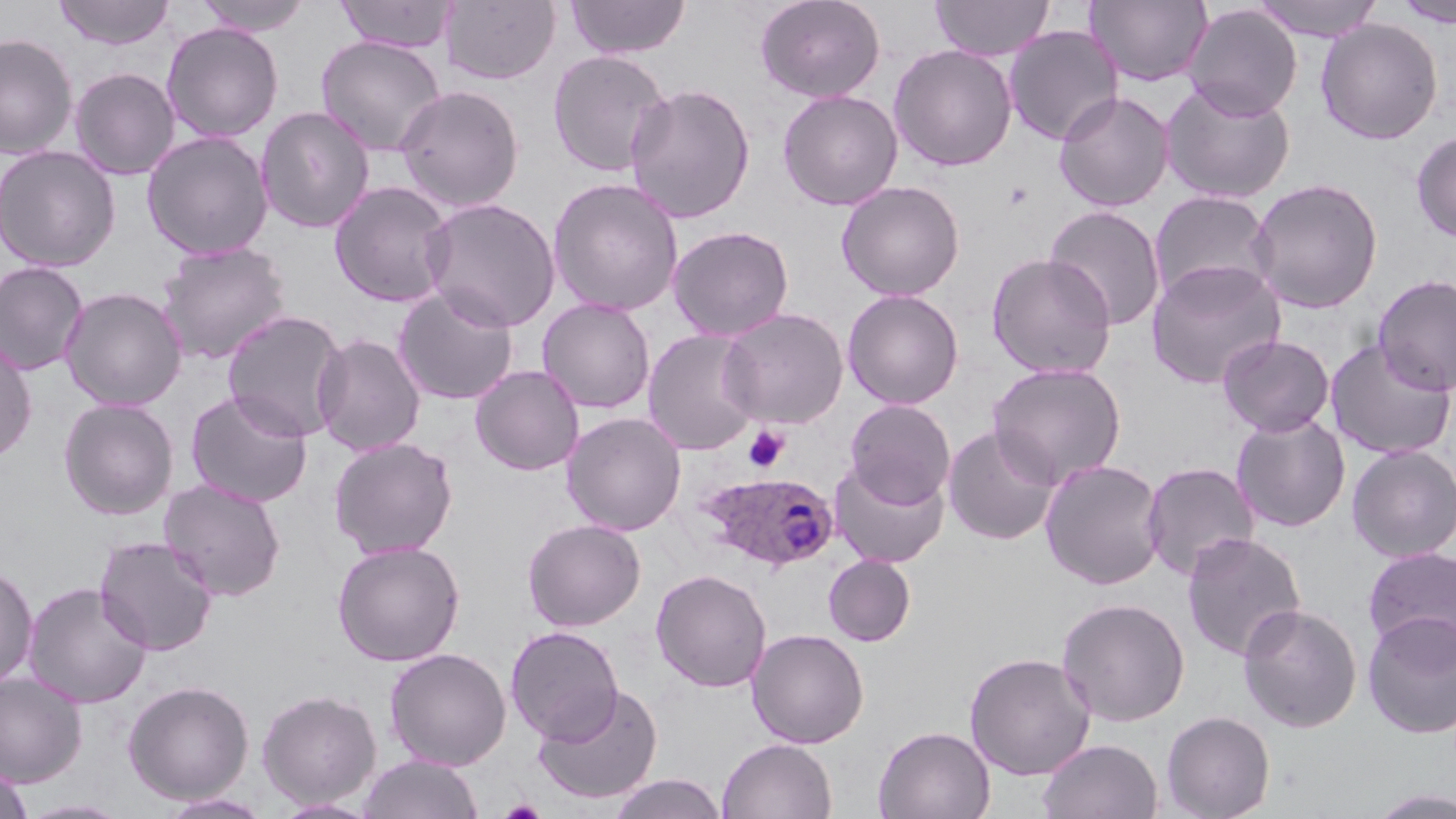
Summary:
  - Coordinate format: approximate bounding boxes as named x1/y1/x2/y2 corners in pixels
  - Platelet locations: (x1=744, y1=426, x2=789, y2=472)
  - Plasmodium ovale-infected red blood cell locations: (x1=696, y1=472, x2=839, y2=571)
  - Uninfected red blood cell locations: (x1=53, y1=0, x2=175, y2=50), (x1=193, y1=0, x2=313, y2=36), (x1=334, y1=0, x2=458, y2=53), (x1=566, y1=0, x2=691, y2=59), (x1=755, y1=0, x2=886, y2=102), (x1=931, y1=0, x2=1054, y2=61), (x1=1085, y1=0, x2=1213, y2=87), (x1=1251, y1=0, x2=1384, y2=41), (x1=440, y1=1, x2=561, y2=86), (x1=1394, y1=1, x2=1456, y2=28), (x1=1183, y1=4, x2=1302, y2=120), (x1=1316, y1=18, x2=1443, y2=145), (x1=161, y1=22, x2=283, y2=143), (x1=1003, y1=26, x2=1123, y2=146), (x1=0, y1=33, x2=78, y2=159), (x1=316, y1=36, x2=446, y2=157), (x1=888, y1=44, x2=1018, y2=172), (x1=547, y1=50, x2=671, y2=177), (x1=69, y1=67, x2=180, y2=180), (x1=1159, y1=80, x2=1296, y2=204), (x1=624, y1=83, x2=756, y2=224), (x1=394, y1=84, x2=524, y2=212), (x1=777, y1=89, x2=903, y2=210), (x1=1053, y1=90, x2=1175, y2=212), (x1=255, y1=105, x2=375, y2=234), (x1=1411, y1=130, x2=1456, y2=243), (x1=141, y1=131, x2=274, y2=259), (x1=0, y1=144, x2=121, y2=273), (x1=548, y1=177, x2=685, y2=316), (x1=1248, y1=177, x2=1384, y2=314), (x1=836, y1=180, x2=965, y2=301), (x1=330, y1=181, x2=455, y2=307), (x1=1149, y1=190, x2=1276, y2=306), (x1=421, y1=197, x2=561, y2=332), (x1=1044, y1=205, x2=1167, y2=330), (x1=667, y1=225, x2=794, y2=341), (x1=157, y1=242, x2=292, y2=364), (x1=985, y1=253, x2=1117, y2=379), (x1=1145, y1=259, x2=1286, y2=389), (x1=0, y1=261, x2=90, y2=376), (x1=1373, y1=273, x2=1456, y2=397), (x1=392, y1=286, x2=520, y2=405), (x1=59, y1=287, x2=188, y2=411), (x1=842, y1=288, x2=964, y2=409), (x1=537, y1=297, x2=656, y2=414), (x1=717, y1=307, x2=849, y2=429), (x1=221, y1=310, x2=348, y2=442), (x1=643, y1=329, x2=763, y2=455), (x1=312, y1=333, x2=426, y2=456), (x1=1217, y1=334, x2=1335, y2=437), (x1=0, y1=338, x2=37, y2=463), (x1=1326, y1=338, x2=1455, y2=460), (x1=987, y1=362, x2=1127, y2=487), (x1=470, y1=364, x2=585, y2=475), (x1=184, y1=389, x2=314, y2=508), (x1=58, y1=398, x2=179, y2=520), (x1=845, y1=400, x2=956, y2=507), (x1=561, y1=412, x2=686, y2=536), (x1=1231, y1=412, x2=1351, y2=533), (x1=943, y1=424, x2=1060, y2=545), (x1=328, y1=437, x2=459, y2=559), (x1=1347, y1=443, x2=1456, y2=562), (x1=829, y1=459, x2=950, y2=569), (x1=1040, y1=459, x2=1167, y2=589), (x1=1141, y1=461, x2=1259, y2=581), (x1=158, y1=478, x2=287, y2=601), (x1=523, y1=519, x2=646, y2=631), (x1=1181, y1=532, x2=1307, y2=661), (x1=94, y1=536, x2=218, y2=656), (x1=331, y1=539, x2=466, y2=666), (x1=1362, y1=546, x2=1456, y2=660), (x1=823, y1=554, x2=916, y2=647), (x1=0, y1=564, x2=38, y2=688), (x1=650, y1=569, x2=772, y2=693), (x1=23, y1=582, x2=152, y2=709), (x1=1056, y1=597, x2=1190, y2=727), (x1=1237, y1=604, x2=1362, y2=733), (x1=1362, y1=611, x2=1456, y2=739), (x1=506, y1=625, x2=624, y2=743), (x1=747, y1=627, x2=869, y2=748), (x1=384, y1=647, x2=512, y2=770), (x1=965, y1=652, x2=1096, y2=780), (x1=0, y1=672, x2=86, y2=787), (x1=122, y1=680, x2=255, y2=804), (x1=363, y1=681, x2=501, y2=817), (x1=532, y1=683, x2=664, y2=805), (x1=256, y1=689, x2=381, y2=808), (x1=1161, y1=711, x2=1276, y2=819), (x1=874, y1=725, x2=995, y2=819), (x1=717, y1=738, x2=837, y2=819), (x1=1037, y1=738, x2=1163, y2=819), (x1=357, y1=754, x2=483, y2=819), (x1=0, y1=767, x2=34, y2=819), (x1=606, y1=773, x2=728, y2=819), (x1=1366, y1=789, x2=1456, y2=818), (x1=158, y1=792, x2=272, y2=818), (x1=19, y1=798, x2=133, y2=818), (x1=270, y1=798, x2=381, y2=818)
  - Slide-level diagnosis: Plasmodium ovale
  - Modality: light microscopy
  - Stain: May-Grünwald-Giemsa
  - Image size: 1456×819 pixels
  - Magnification: 1000x
  - Field of view: single
  - Preparation: thin blood film